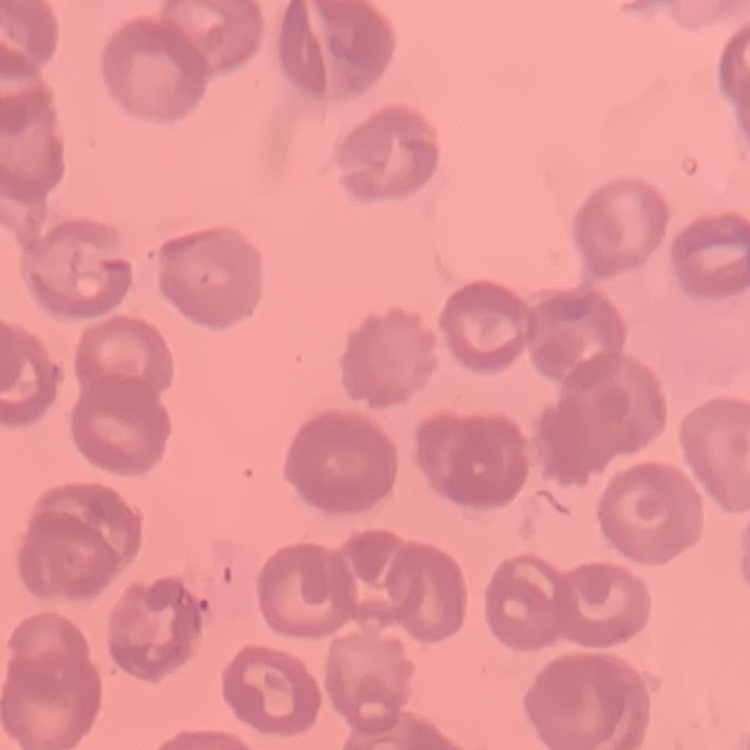
erythrocyte_morphology: no rouleaux formation
image_type: one tile cut from a larger photomicrograph
stain: Field's or Giemsa
preparation: thin blood film